Outline each uninfected red blood cell.
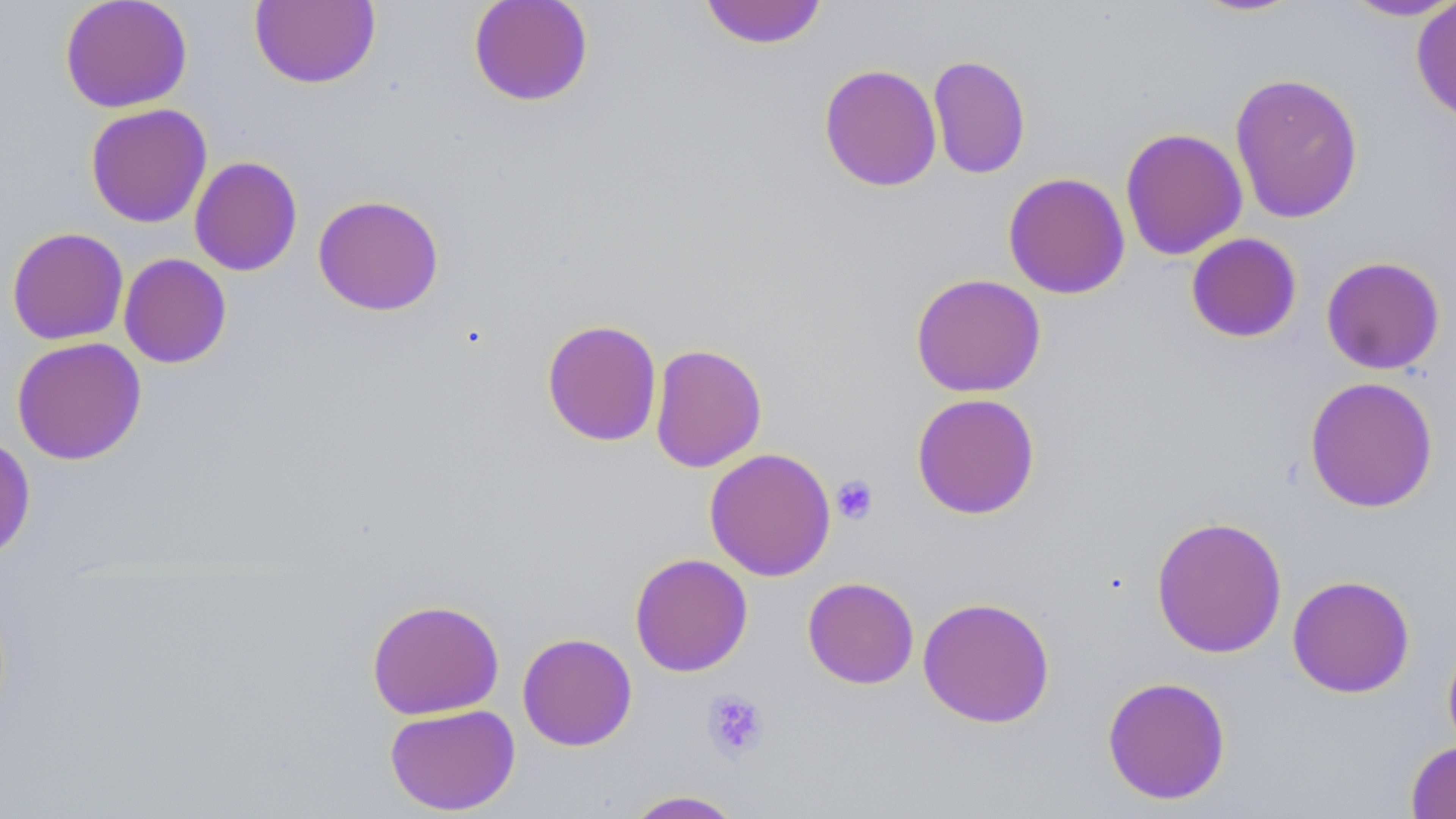
Approximate bounding boxes as [x1, y1, x2, y2] in pixels.
Uninfected red blood cells: [59, 0, 193, 113], [467, 0, 594, 107], [699, 0, 828, 49], [1188, 0, 1306, 18], [1339, 0, 1456, 23], [250, 1, 380, 89], [1411, 2, 1456, 125], [927, 55, 1031, 180], [818, 63, 942, 192], [1229, 72, 1364, 224], [85, 103, 213, 228], [1119, 127, 1247, 261], [189, 156, 303, 277], [1003, 172, 1131, 299], [312, 194, 445, 316], [6, 226, 129, 346], [1185, 232, 1303, 344], [118, 253, 232, 369], [1320, 255, 1446, 375], [910, 273, 1047, 398], [541, 318, 663, 447], [11, 336, 147, 465], [649, 343, 767, 473], [1304, 376, 1439, 513], [911, 392, 1041, 520], [0, 433, 36, 564], [704, 447, 836, 581], [1150, 515, 1288, 659], [629, 553, 753, 677], [1287, 574, 1416, 698], [803, 576, 919, 689], [917, 596, 1055, 728], [366, 598, 504, 720], [517, 632, 638, 751], [1442, 634, 1456, 758], [1102, 675, 1231, 805], [384, 704, 520, 815], [1405, 740, 1456, 819], [622, 789, 747, 818].

slide_level_diagnosis: no evidence of blood parasites
image_size: 1456×819 pixels
field_of_view: one of a larger specimen
modality: optical microscopy
preparation: thin blood smear
stain: May-Grünwald-Giemsa
magnification: 1000x
platelet_locations: 'approximate bounding boxes as [x1, y1, x2, y2] in pixels: [831, 474, 879, 525], [701, 690, 769, 760]'